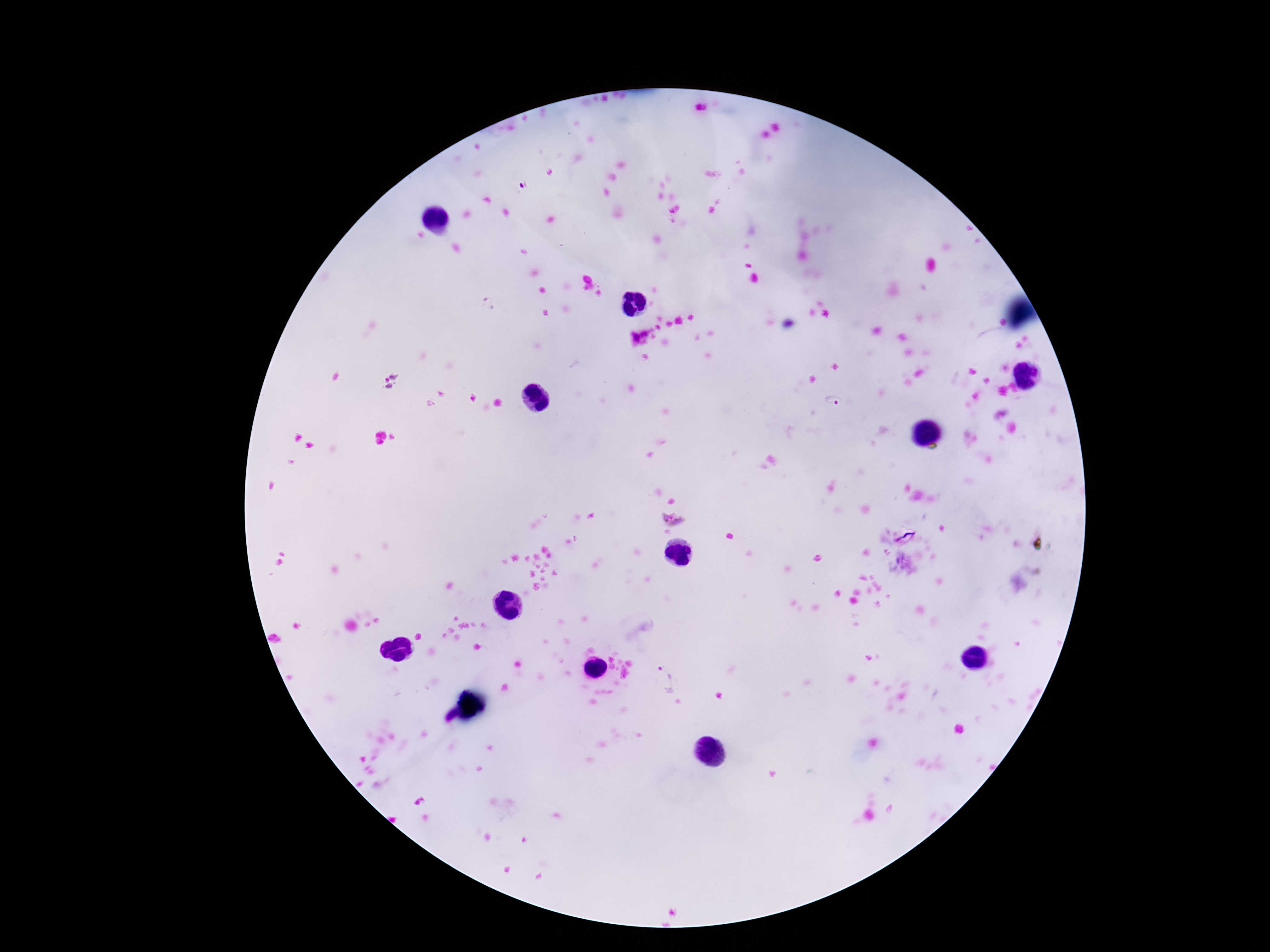

magnification: 100x
patient_malaria_status: infected
plasmodium_parasite_locations: 'approximate centers as {x, y} in pixels: {390, 380}, {832, 401}, {673, 518}, {905, 537}, {665, 677}'
image_size: 1270×952 pixels
preparation: thick peripheral-blood smear
stain: Giemsa
field_of_view: one from this slide
capture: smartphone camera through the microscope eyepiece